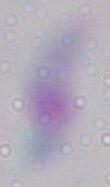

identification = Toxoplasma gondii
magnification = 1000x
modality = photomicrograph